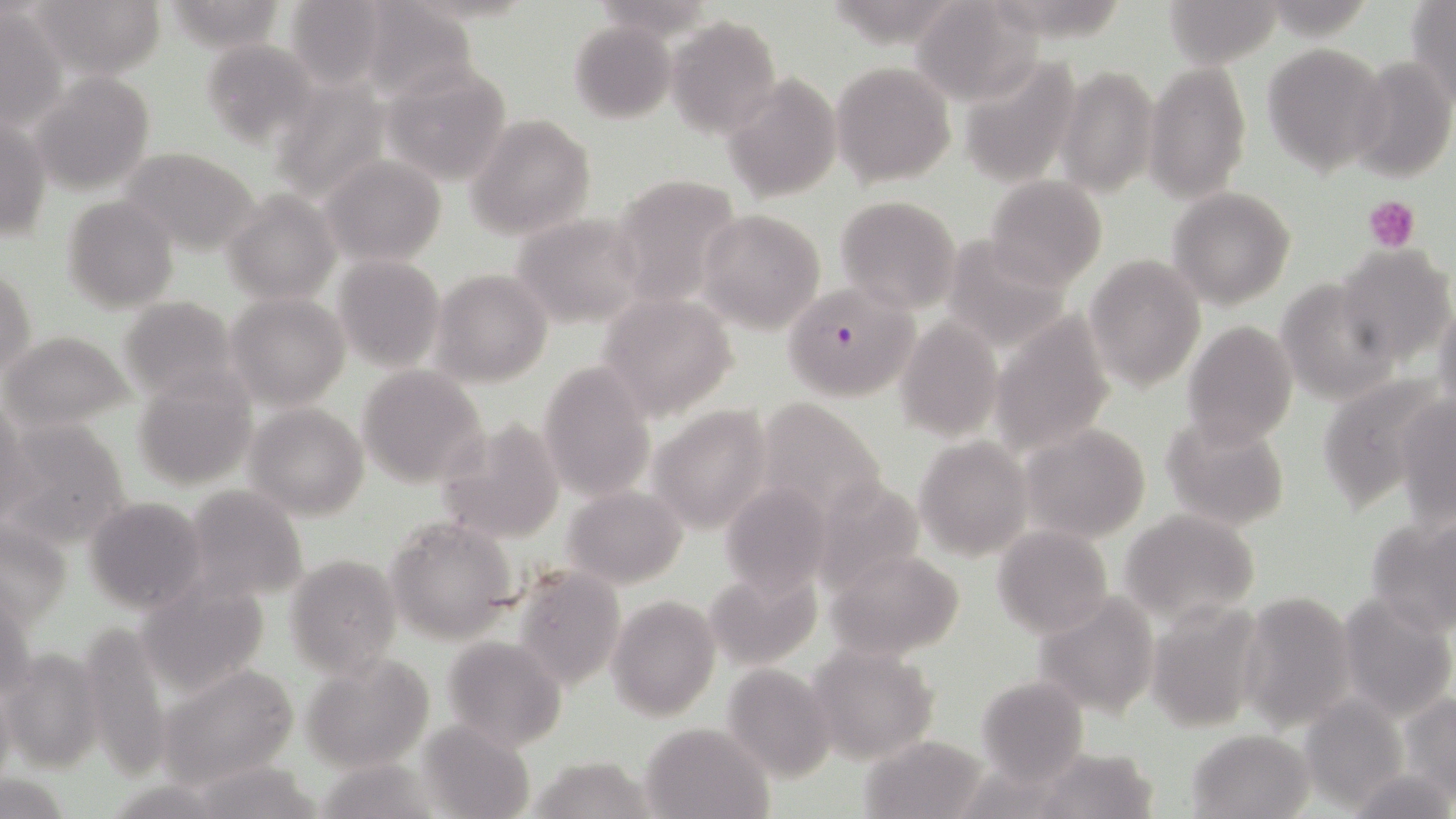 Approximate bounding boxes as named x1/y1/x2/y2 corners in pixels. Plasmodium falciparum-infected red blood cell locations: (x1=779, y1=283, x2=926, y2=406). Uninfected red blood cell locations: (x1=31, y1=0, x2=165, y2=79), (x1=164, y1=0, x2=291, y2=52), (x1=283, y1=0, x2=392, y2=89), (x1=910, y1=0, x2=1043, y2=104), (x1=1163, y1=0, x2=1279, y2=67), (x1=1405, y1=1, x2=1456, y2=103), (x1=357, y1=2, x2=476, y2=105), (x1=1, y1=6, x2=67, y2=130), (x1=666, y1=15, x2=780, y2=137), (x1=569, y1=19, x2=676, y2=124), (x1=198, y1=37, x2=321, y2=148), (x1=1263, y1=42, x2=1388, y2=177), (x1=958, y1=55, x2=1082, y2=187), (x1=1349, y1=55, x2=1455, y2=183), (x1=831, y1=61, x2=957, y2=188), (x1=1142, y1=61, x2=1252, y2=203), (x1=381, y1=63, x2=512, y2=187), (x1=1057, y1=63, x2=1158, y2=198), (x1=30, y1=71, x2=154, y2=195), (x1=266, y1=72, x2=394, y2=201), (x1=722, y1=75, x2=842, y2=202), (x1=468, y1=114, x2=596, y2=239), (x1=1, y1=115, x2=51, y2=243), (x1=120, y1=146, x2=262, y2=256), (x1=321, y1=156, x2=446, y2=267), (x1=612, y1=175, x2=741, y2=300), (x1=984, y1=177, x2=1107, y2=290), (x1=1167, y1=188, x2=1297, y2=310), (x1=222, y1=190, x2=338, y2=305), (x1=61, y1=194, x2=179, y2=312), (x1=834, y1=195, x2=960, y2=313), (x1=698, y1=208, x2=824, y2=335), (x1=510, y1=213, x2=648, y2=328), (x1=942, y1=235, x2=1072, y2=348), (x1=1335, y1=243, x2=1455, y2=366), (x1=333, y1=254, x2=443, y2=371), (x1=1084, y1=255, x2=1205, y2=394), (x1=1, y1=268, x2=36, y2=381), (x1=431, y1=269, x2=554, y2=387), (x1=1277, y1=278, x2=1398, y2=406), (x1=596, y1=291, x2=738, y2=421), (x1=226, y1=292, x2=351, y2=408), (x1=116, y1=295, x2=242, y2=404), (x1=1433, y1=299, x2=1456, y2=418), (x1=987, y1=310, x2=1119, y2=459), (x1=895, y1=318, x2=1003, y2=443), (x1=1182, y1=319, x2=1298, y2=449), (x1=1, y1=330, x2=131, y2=430), (x1=538, y1=362, x2=656, y2=502), (x1=357, y1=366, x2=487, y2=488), (x1=1316, y1=369, x2=1444, y2=507), (x1=133, y1=373, x2=256, y2=489), (x1=1, y1=394, x2=29, y2=522), (x1=754, y1=395, x2=888, y2=519), (x1=1394, y1=396, x2=1455, y2=527), (x1=245, y1=402, x2=369, y2=520), (x1=647, y1=404, x2=775, y2=532), (x1=1163, y1=414, x2=1291, y2=531), (x1=436, y1=419, x2=566, y2=544), (x1=4, y1=420, x2=132, y2=548), (x1=1019, y1=423, x2=1152, y2=543), (x1=914, y1=438, x2=1030, y2=558), (x1=809, y1=475, x2=926, y2=594), (x1=720, y1=480, x2=833, y2=595), (x1=182, y1=485, x2=307, y2=603), (x1=561, y1=485, x2=689, y2=589), (x1=84, y1=496, x2=206, y2=612), (x1=1120, y1=509, x2=1259, y2=624), (x1=1365, y1=513, x2=1456, y2=636), (x1=386, y1=517, x2=517, y2=643), (x1=1, y1=520, x2=72, y2=626), (x1=991, y1=525, x2=1113, y2=638), (x1=825, y1=548, x2=966, y2=662), (x1=285, y1=555, x2=403, y2=677), (x1=511, y1=563, x2=626, y2=690), (x1=705, y1=564, x2=823, y2=672), (x1=137, y1=580, x2=268, y2=695), (x1=1238, y1=590, x2=1358, y2=730), (x1=1336, y1=591, x2=1455, y2=719), (x1=1034, y1=593, x2=1163, y2=717), (x1=608, y1=595, x2=720, y2=721), (x1=1148, y1=601, x2=1267, y2=731), (x1=74, y1=619, x2=170, y2=774), (x1=441, y1=637, x2=566, y2=751), (x1=808, y1=644, x2=941, y2=766), (x1=0, y1=647, x2=105, y2=773), (x1=299, y1=655, x2=436, y2=772), (x1=157, y1=662, x2=302, y2=788), (x1=722, y1=663, x2=837, y2=781), (x1=976, y1=676, x2=1089, y2=782), (x1=1399, y1=692, x2=1456, y2=799), (x1=1300, y1=696, x2=1406, y2=812), (x1=419, y1=721, x2=533, y2=818), (x1=639, y1=721, x2=773, y2=818), (x1=1187, y1=728, x2=1314, y2=817), (x1=859, y1=733, x2=989, y2=817), (x1=1029, y1=746, x2=1158, y2=819), (x1=527, y1=756, x2=662, y2=819), (x1=314, y1=758, x2=443, y2=818), (x1=188, y1=762, x2=326, y2=819), (x1=1349, y1=766, x2=1454, y2=819), (x1=1, y1=776, x2=70, y2=816). Platelet locations: (x1=1364, y1=195, x2=1420, y2=253). Slide-level diagnosis: Plasmodium falciparum. 1000x magnification. May-Grünwald-Giemsa-stained preparation. One field of a larger specimen. Thin blood film. Image is 1456×819 pixels. Optical microscopy.